Identify the parasite.
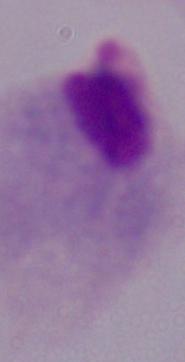
A trichomonad.

Summary:
  - Magnification: 1000x
  - Modality: photomicrograph